Locate every Plasmodium parasite and identify its life-cycle stage.
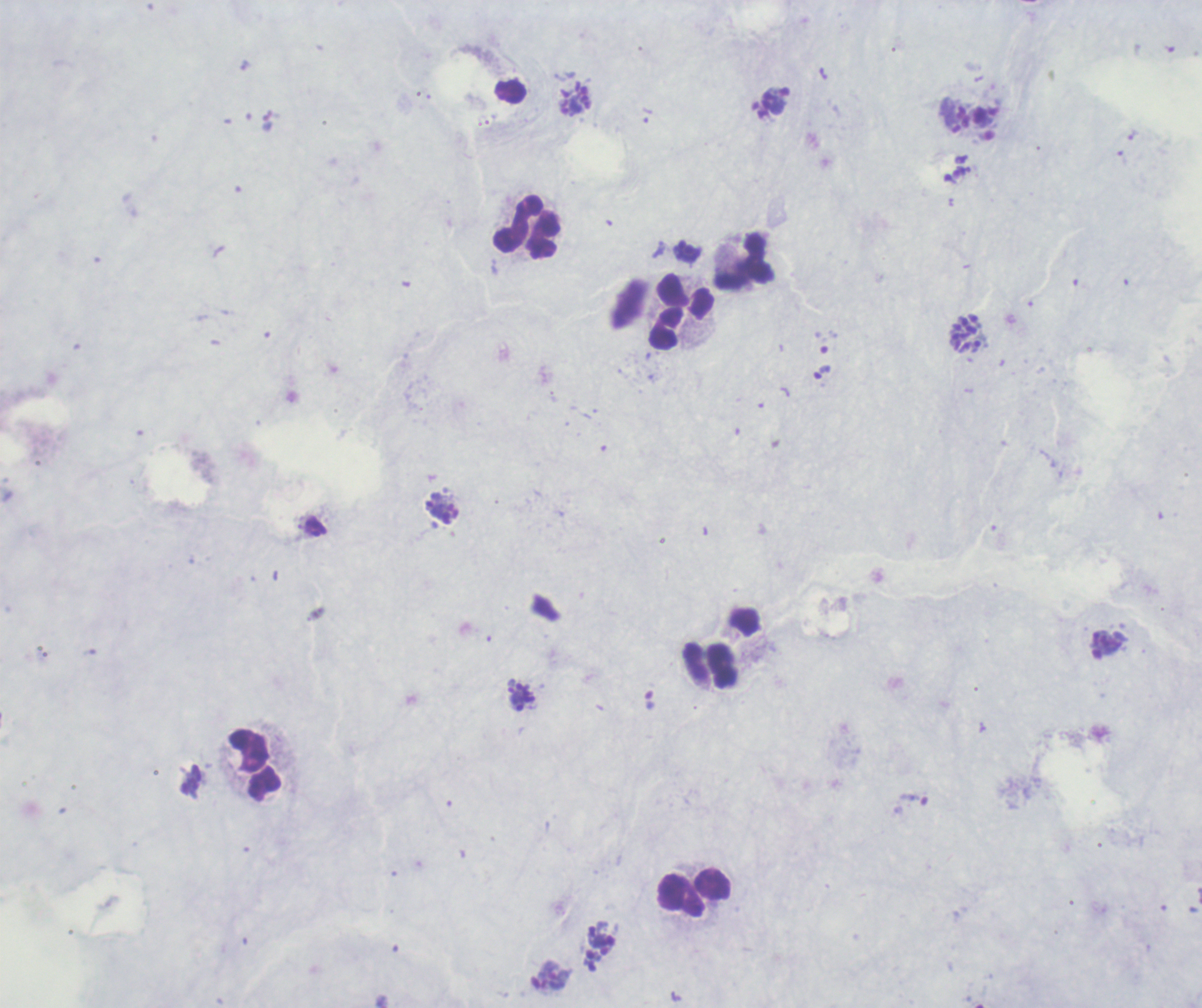
Approximate centers as (x, y) in pixels.
Schizonts: (575, 98), (965, 334), (442, 508), (521, 696), (600, 948).
No trophozoite or gametocyte forms observed.

Approximate centers as (x, y) in pixels. Leukocyte locations: (526, 228), (745, 260), (682, 313), (712, 665), (255, 765), (696, 894). Captured at 100x magnification. Romanowsky-stained preparation. One field from this slide. Previously used in an actual diagnosis. Background quality: poor. Image is 1202×1008 pixels. Thick blood smear.